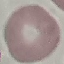
result = no malaria parasites detected
capture = smartphone camera at the microscope eyepiece
stain = Giemsa
image type = cell patch, automatically extracted from a larger field of view and resized to 64 × 64 pixels
preparation = thin blood film